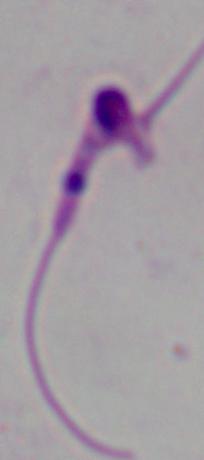

{
  "identification": "Leishmania",
  "modality": "photomicrograph",
  "magnification": "1000x"
}